Assess this cell for malaria.
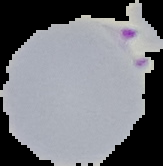

Parasitized.

image type = segmented cell region on a black background
preparation = thin blood film
image size = 163×166 pixels